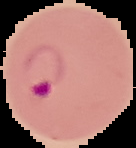
image type = segmented cell region on a black background
preparation = thin blood smear
image size = 136×148 pixels
malaria status = parasitized